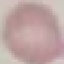
result = no malaria parasites detected
image type = automatically extracted cell patch, resized to 64 × 64 pixels
stain = Giemsa
preparation = thin blood smear
capture = smartphone camera at the microscope eyepiece